Locate malaria parasites and leukocytes.
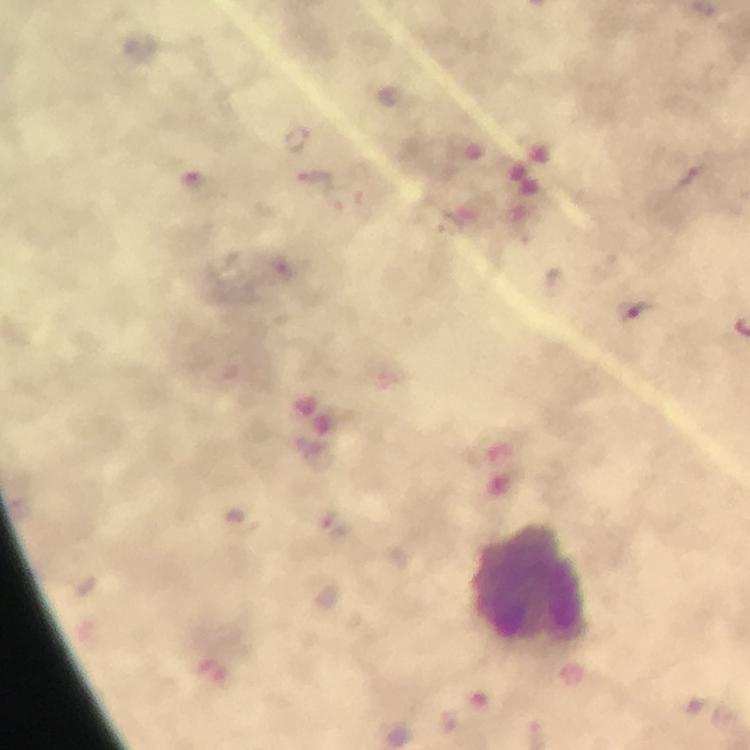

Approximate object centers, in pixels from the top-left corner.
Malaria parasites: (x=296, y=138), (x=315, y=182), (x=193, y=183), (x=281, y=267), (x=634, y=309), (x=335, y=525).
Leukocytes: (x=527, y=586).

Giemsa stain. Image is 750×750 pixels. Cropped region of a single field of view. Photographed with a smartphone mounted on the microscope. Immersion oil was used. 100x magnification. From a diagnostic examination for malaria. Thick blood film.